Outline each blood parasite and name the species.
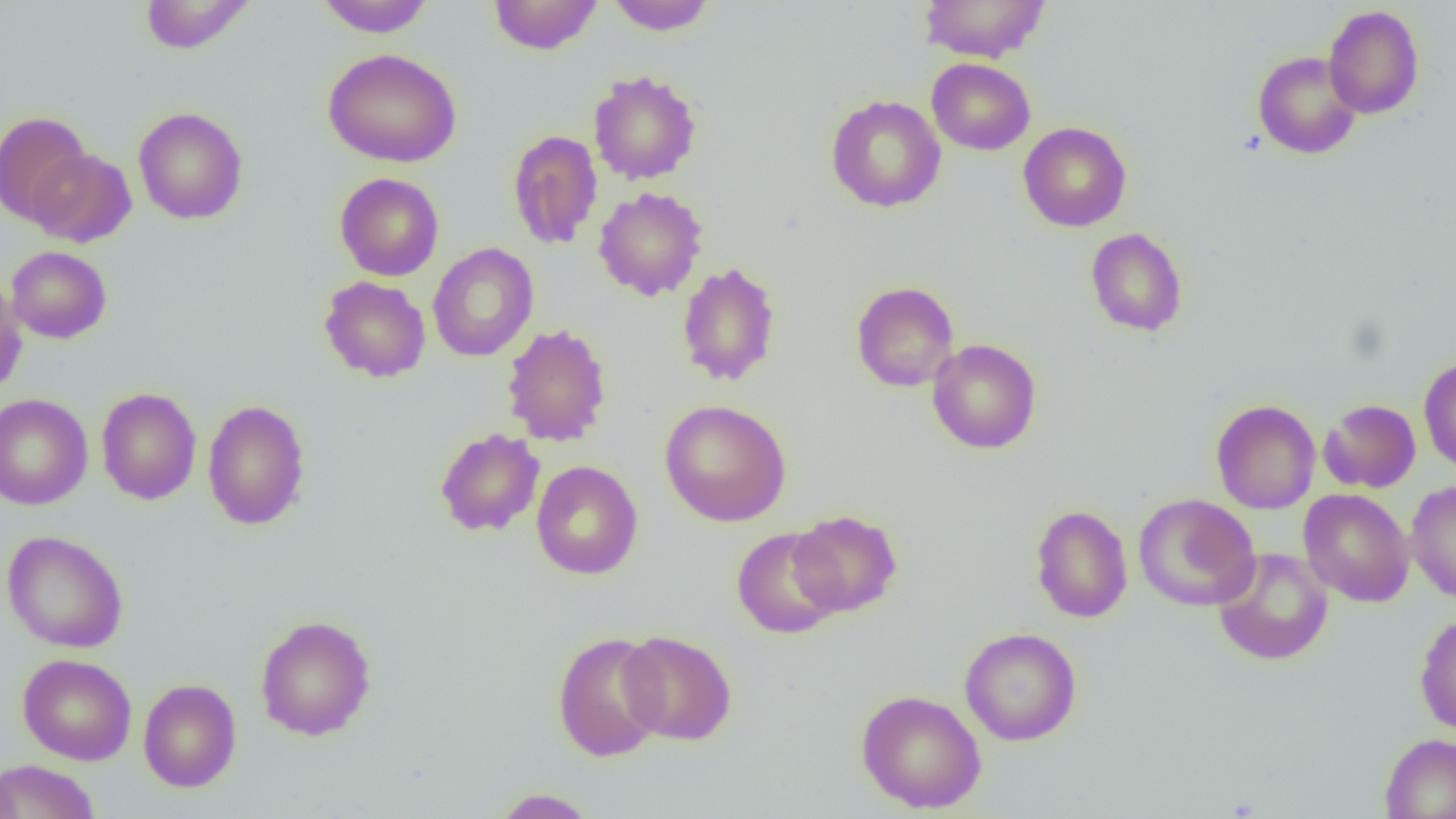
No blood parasites seen.

slide_level_diagnosis: negative for blood parasites
image_size: 1456×819 pixels
field_of_view: one of a larger specimen
magnification: 1000x
modality: light microscopy
preparation: thin blood film
uninfected_red_blood_cell_locations: 'approximate bounding boxes as (x1, y1, x2, y2) in pixels: (139, 0, 255, 54), (315, 0, 436, 37), (488, 0, 603, 55), (606, 0, 717, 35), (919, 0, 1051, 63), (1323, 5, 1424, 119), (322, 48, 461, 168), (1252, 50, 1362, 159), (927, 58, 1036, 155), (588, 70, 702, 185), (825, 94, 946, 213), (133, 106, 248, 224), (0, 111, 92, 226), (1018, 122, 1131, 232), (507, 129, 603, 249), (27, 148, 136, 247), (334, 173, 444, 281), (593, 186, 708, 301), (1085, 227, 1188, 337), (427, 243, 539, 362), (6, 246, 112, 343), (677, 261, 782, 387), (319, 276, 431, 383), (0, 277, 27, 396), (851, 281, 960, 392), (501, 323, 612, 447), (927, 338, 1041, 454), (1418, 356, 1456, 475), (96, 387, 201, 505), (0, 393, 93, 510), (202, 399, 311, 531), (660, 399, 791, 526), (1211, 399, 1320, 514), (1319, 399, 1421, 493), (434, 428, 544, 537), (531, 460, 643, 579), (1405, 480, 1456, 604), (1299, 488, 1414, 607), (1133, 494, 1260, 611), (1030, 505, 1133, 623), (788, 509, 902, 617), (732, 527, 845, 639), (2, 530, 128, 652), (1212, 546, 1334, 666), (1414, 613, 1456, 735), (255, 614, 377, 741), (959, 627, 1082, 746), (551, 630, 667, 763), (617, 630, 737, 745), (17, 653, 137, 765), (138, 679, 242, 792), (856, 689, 986, 813), (1379, 732, 1456, 819), (0, 759, 100, 819), (491, 788, 598, 818)'